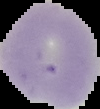

Summary:
  - Image size: 100×109 pixels
  - Image type: segmented cell region on a black background
  - Malaria status: uninfected
  - Preparation: thin blood smear